State which cell type is depicted.
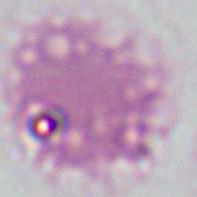

This is an erythrocyte.

magnification = 1000x
modality = photomicrograph